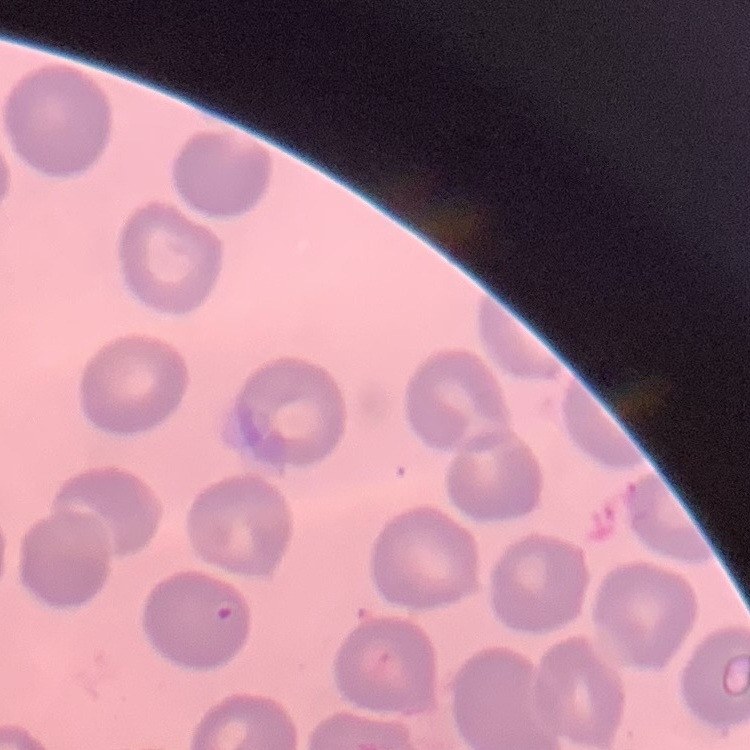

{
  "red_blood_cell_morphology": "no rouleaux formation",
  "image_type": "one tile cut from a larger photomicrograph",
  "stain": "Field's or Giemsa",
  "preparation": "thin peripheral smear"
}